State which parasite is depicted.
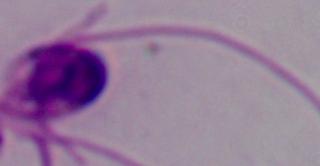
This is Leishmania.

Summary:
  - Modality: micrograph
  - Magnification: 1000x